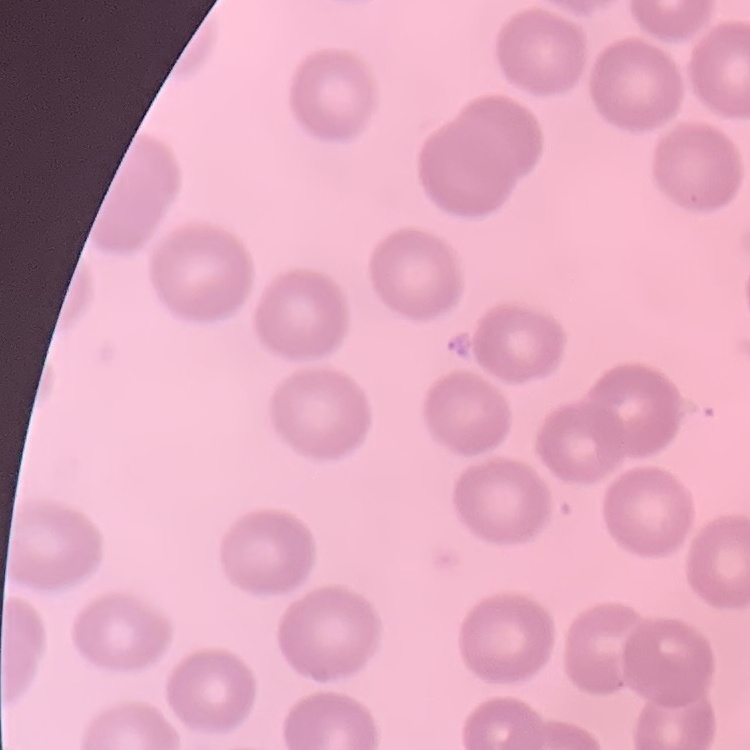

erythrocyte morphology = no rouleaux formation
preparation = thin peripheral smear
stain = Field's or Giemsa
image type = one tile cut from a larger photomicrograph